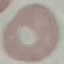

Summary:
  - Result: no malaria parasites seen
  - Preparation: thin blood smear
  - Stain: Giemsa
  - Capture: smartphone through the microscope eyepiece
  - Image type: automatically extracted cell patch, resized to 64 × 64 pixels